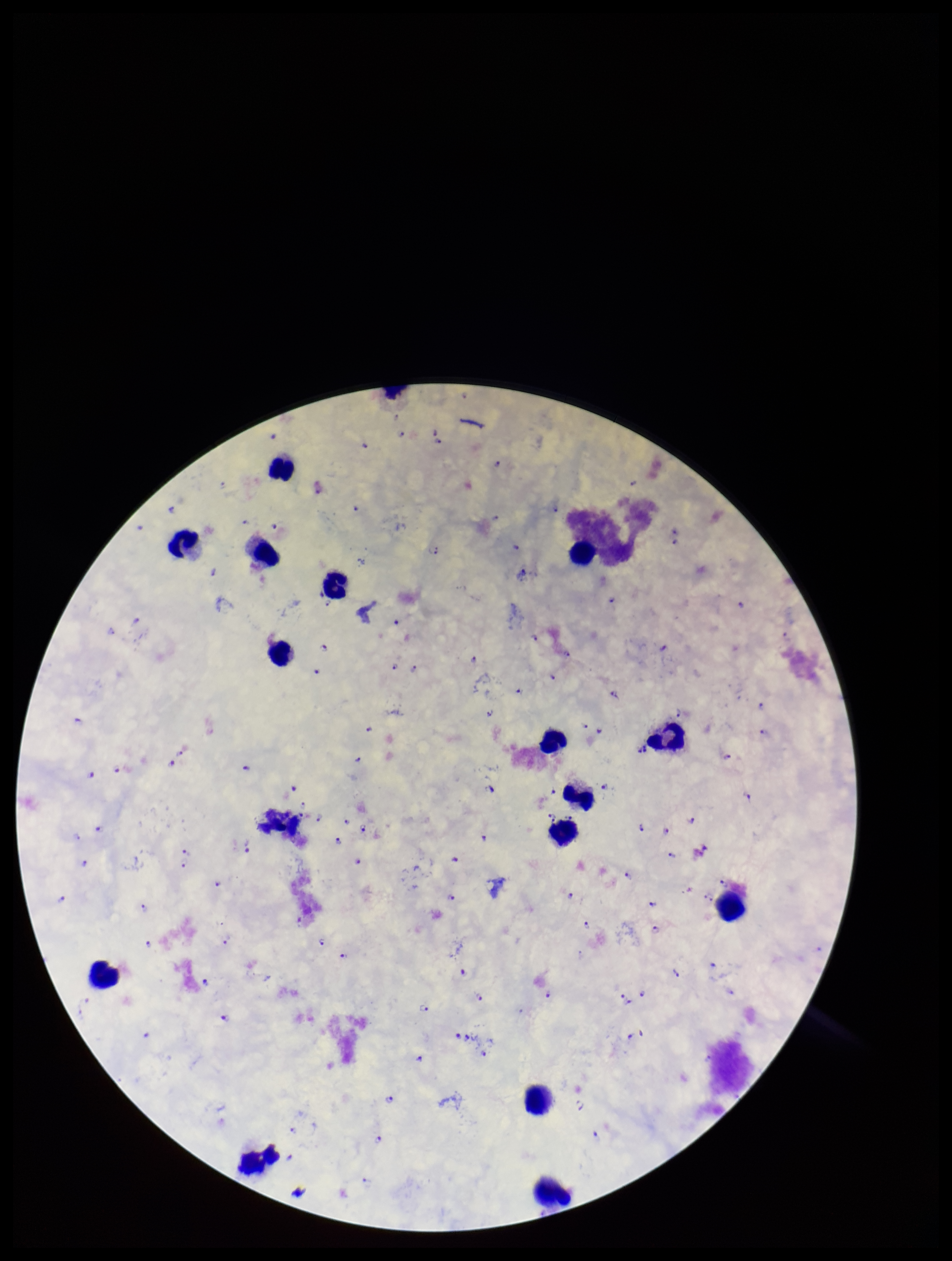
field_of_view: single
plasmodium_parasites: identified
preparation: thick
parasite_count: 131
leukocyte_count: 15
species_reported_for_this_patient: Plasmodium falciparum
capture: smartphone photograph through the microscope eyepiece
image_size: 952×1261 pixels
stain: Giemsa
patient_malaria_status: positive